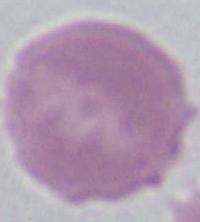

Summary:
  - Modality: micrograph
  - Identification: red blood cell
  - Magnification: 1000x